Report the malaria status of this cell.
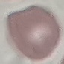

It is uninfected.

capture = smartphone camera at the microscope eyepiece
image type = automatically extracted cell patch, resized to 64 × 64 pixels
preparation = thin smear
stain = Giemsa